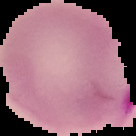

Summary:
  - Malaria status: parasitized
  - Image type: segmented cell region with the area outside set to black
  - Image size: 136×136 pixels
  - Preparation: thin blood smear